Give the position of every malaria parasite.
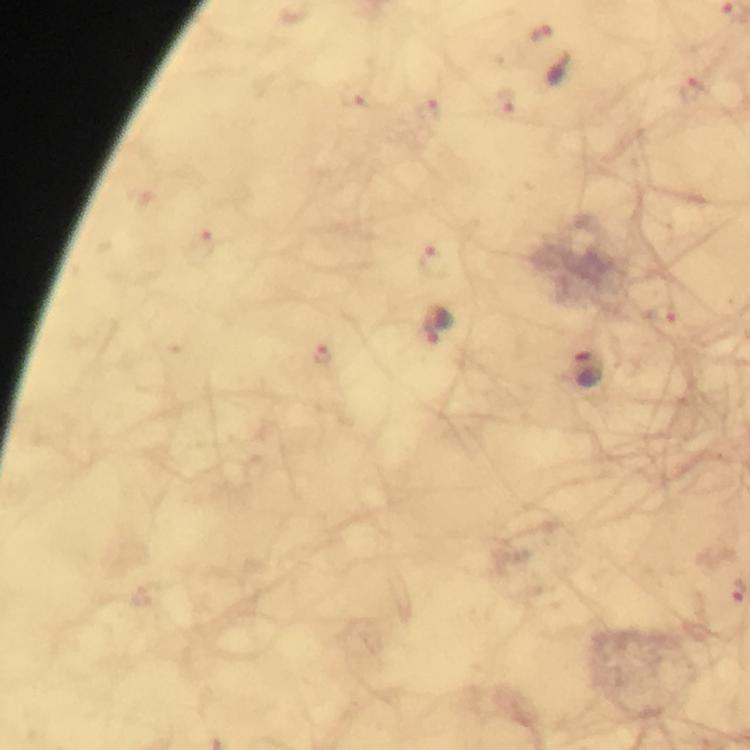
Approximate object centers, in pixels from the top-left corner.
Malaria parasites: (x=540, y=34), (x=696, y=91), (x=354, y=95), (x=507, y=103), (x=430, y=111), (x=202, y=247), (x=432, y=262), (x=669, y=321), (x=323, y=355), (x=587, y=368), (x=736, y=593).

magnification = 100x
preparation = thick blood smear
stain = Giemsa
capture = smartphone photograph through a microscope
context = from a diagnostic examination for malaria
image size = 750×750 pixels
immersion oil = applied
cropped from = a single field of view